Comment on the morphology of the erythrocytes.
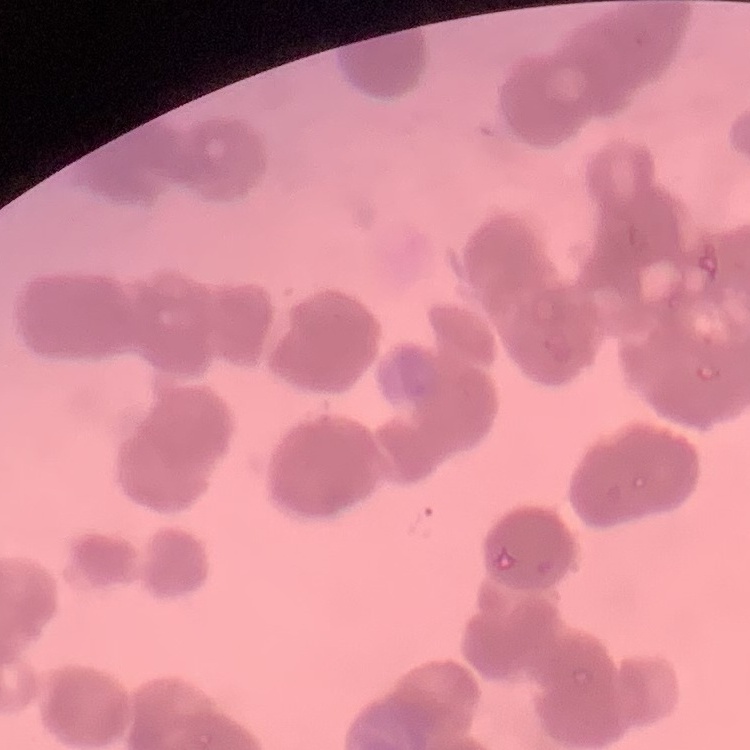

They show rouleaux formation.

One tile cut from a larger photomicrograph. Field's or Giemsa stain. Thin peripheral smear.